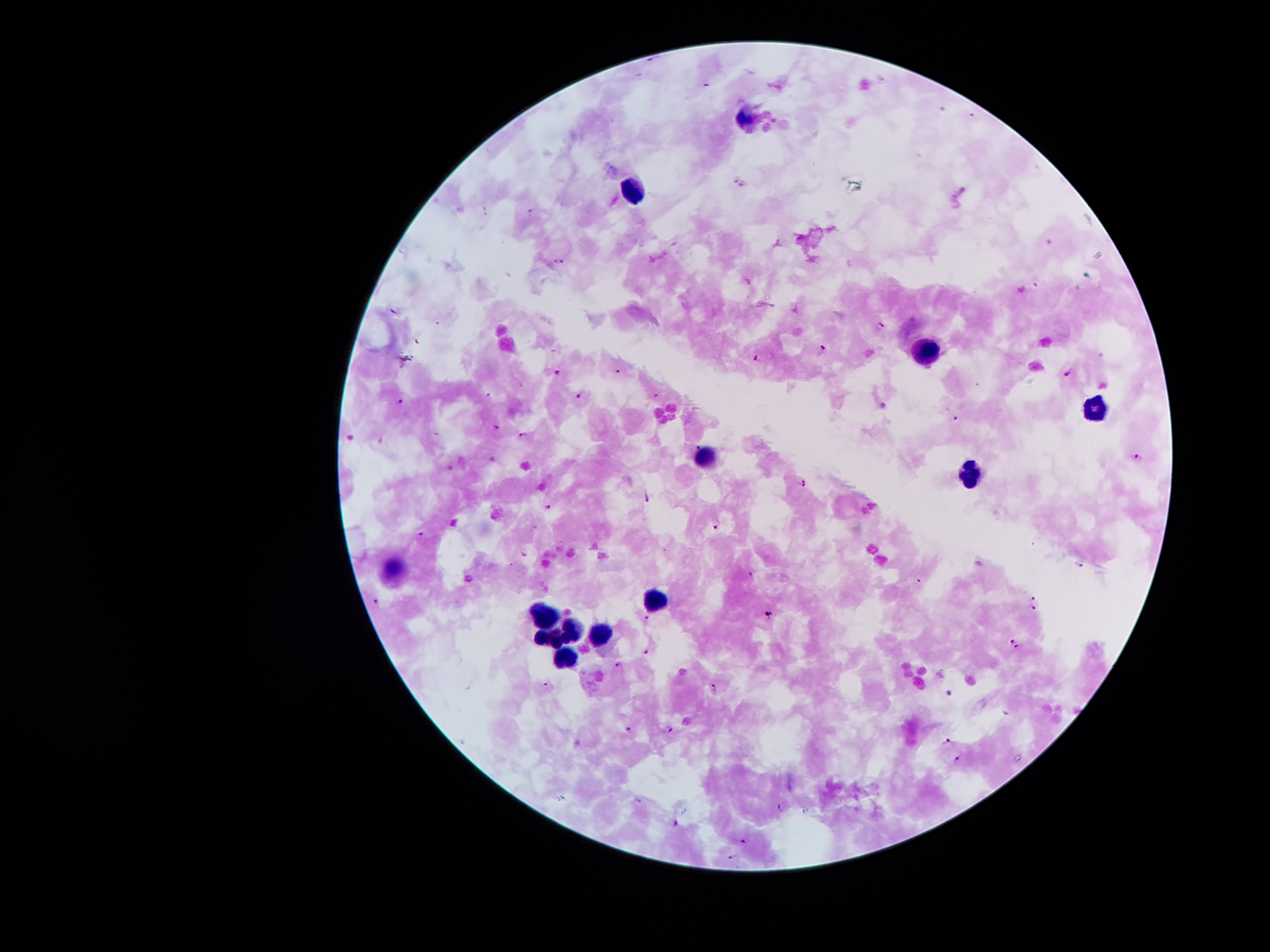 Approximate object centers, in pixels from the top-left corner. Leukocyte locations: (x=743, y=117), (x=634, y=189), (x=921, y=351), (x=1098, y=410), (x=706, y=456), (x=975, y=475), (x=655, y=599), (x=547, y=614), (x=575, y=630), (x=600, y=633), (x=549, y=635), (x=566, y=654). Malaria parasite locations: (x=707, y=83), (x=559, y=260), (x=879, y=327), (x=823, y=348), (x=758, y=356), (x=618, y=371), (x=1070, y=371), (x=558, y=372), (x=657, y=394), (x=580, y=396), (x=401, y=400), (x=957, y=419), (x=498, y=425), (x=523, y=436), (x=698, y=446), (x=1138, y=457), (x=805, y=481), (x=648, y=496), (x=547, y=504), (x=718, y=524), (x=421, y=534), (x=524, y=552), (x=752, y=574), (x=1033, y=597), (x=375, y=601), (x=1033, y=607), (x=647, y=618), (x=1013, y=641), (x=1017, y=647), (x=646, y=651), (x=618, y=663), (x=546, y=684), (x=714, y=687), (x=950, y=694), (x=628, y=728), (x=669, y=729), (x=949, y=741), (x=956, y=758), (x=781, y=808), (x=674, y=822), (x=745, y=840), (x=732, y=855). Image is 1270×952 pixels. Patient malaria status: infected with Plasmodium falciparum. Thick blood film. 100x magnification. Giemsa stain. Photographed through the microscope eyepiece with a smartphone camera. Single field of view.